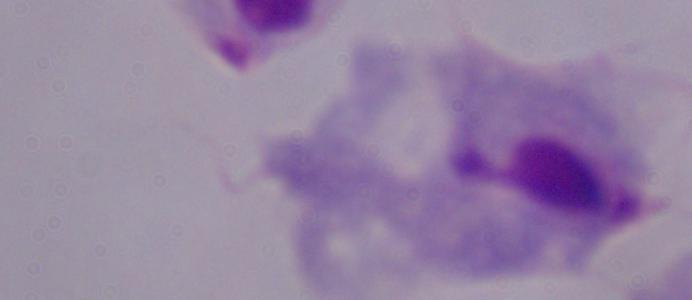

identification = trichomonad
modality = photomicrograph
magnification = 1000x